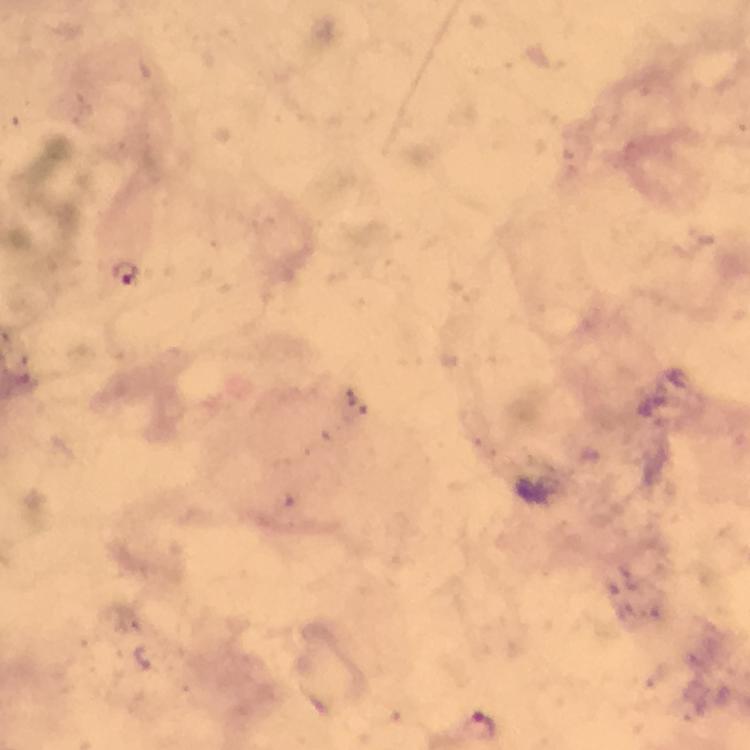
malaria_parasite_locations: 'approximate centers as (x, y) in pixels: (128, 272), (484, 725)'
capture: smartphone camera through the microscope
cropped_from: a single field of view
preparation: thick smear
image_size: 750×750 pixels
immersion_oil: applied
context: from a diagnostic examination for malaria
stain: Giemsa
magnification: 100x